Locate Plasmodium parasites and leukocytes.
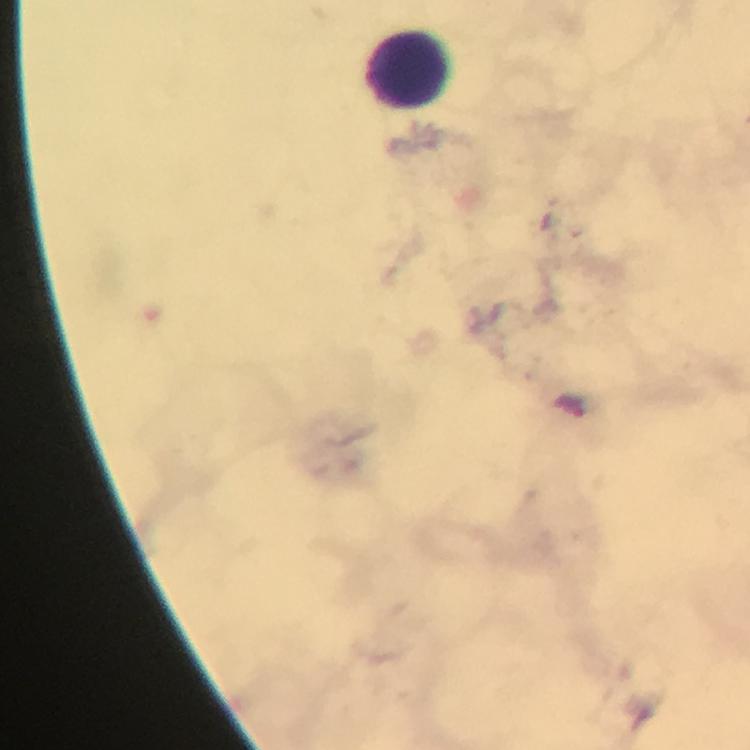
Approximate centers as {x, y} in pixels.
Plasmodium parasites: {572, 406}.
Leukocytes: {409, 68}.

stain = Giemsa
context = from a diagnostic examination for malaria
cropped from = a single field of view
capture = smartphone mounted on the microscope
preparation = thick blood film
immersion oil = applied
magnification = 100x
image size = 750×750 pixels